Locate every Plasmodium parasite.
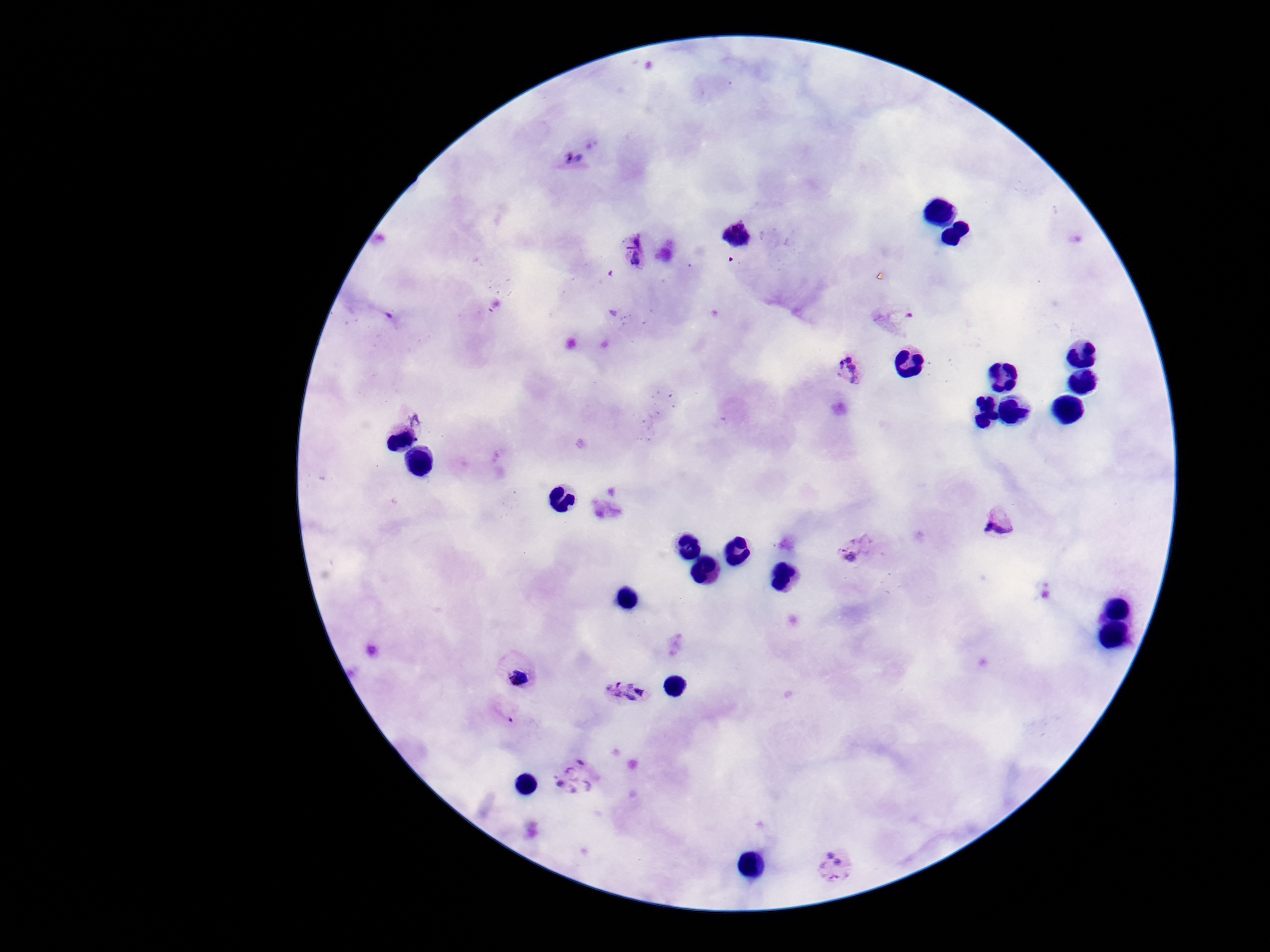

Approximate object centers, in pixels from the top-left corner.
Plasmodium parasites: (x=574, y=158), (x=736, y=235), (x=631, y=251), (x=895, y=315), (x=848, y=368), (x=414, y=417), (x=1000, y=516), (x=861, y=551), (x=513, y=670), (x=628, y=694), (x=501, y=714), (x=575, y=778), (x=838, y=867).

Image is 1270×952 pixels. Patient malaria status: infected. Giemsa-stained preparation. Single field of view. Thick blood film. Smartphone photograph taken through the microscope eyepiece. 100x magnification.